Assess this cell for malaria.
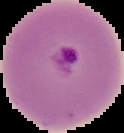
Parasitized.

{
  "image_size": "124×133 pixels",
  "preparation": "thin blood smear",
  "image_type": "segmented cell region on a black background"
}